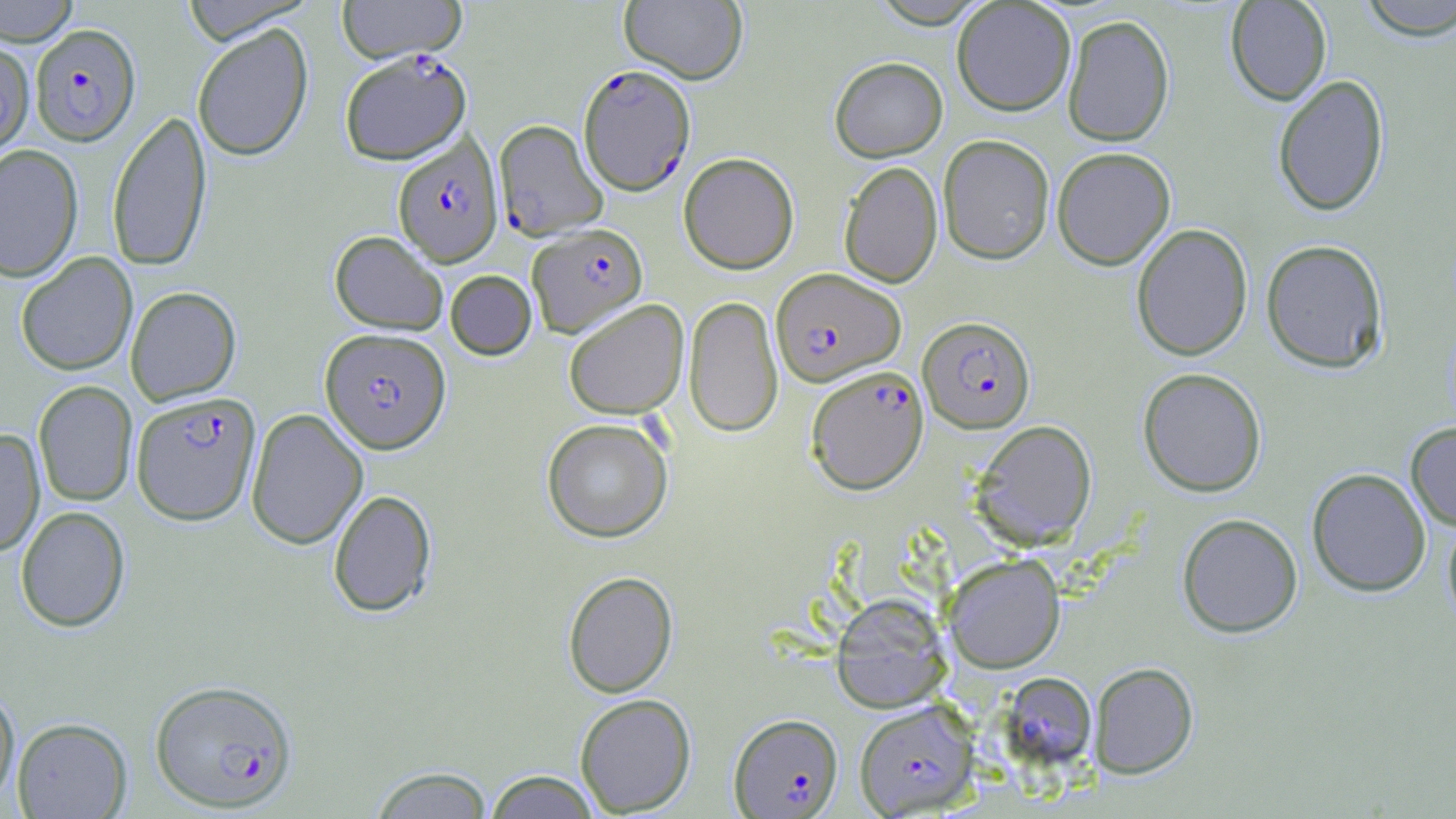

Approximate bounding boxes as named x1/y1/x2/y2 corners in pixels. Uninfected red blood cell locations: (x1=0, y1=0, x2=80, y2=45), (x1=336, y1=0, x2=466, y2=64), (x1=619, y1=0, x2=748, y2=84), (x1=869, y1=0, x2=992, y2=28), (x1=1225, y1=0, x2=1332, y2=105), (x1=1354, y1=0, x2=1456, y2=40), (x1=179, y1=1, x2=316, y2=45), (x1=952, y1=1, x2=1076, y2=116), (x1=1062, y1=14, x2=1175, y2=147), (x1=191, y1=24, x2=313, y2=161), (x1=0, y1=39, x2=35, y2=158), (x1=829, y1=56, x2=947, y2=162), (x1=1273, y1=74, x2=1389, y2=216), (x1=106, y1=109, x2=212, y2=272), (x1=938, y1=134, x2=1055, y2=264), (x1=0, y1=144, x2=83, y2=282), (x1=1052, y1=147, x2=1176, y2=270), (x1=678, y1=152, x2=799, y2=274), (x1=839, y1=161, x2=943, y2=288), (x1=1131, y1=223, x2=1253, y2=360), (x1=330, y1=231, x2=448, y2=335), (x1=1261, y1=239, x2=1388, y2=373), (x1=16, y1=252, x2=138, y2=376), (x1=445, y1=270, x2=537, y2=359), (x1=125, y1=286, x2=241, y2=405), (x1=683, y1=295, x2=783, y2=437), (x1=563, y1=299, x2=688, y2=419), (x1=1137, y1=367, x2=1266, y2=497), (x1=33, y1=380, x2=137, y2=506), (x1=246, y1=408, x2=368, y2=550), (x1=541, y1=418, x2=673, y2=542), (x1=970, y1=420, x2=1097, y2=550), (x1=1406, y1=422, x2=1456, y2=530), (x1=0, y1=428, x2=45, y2=556), (x1=1307, y1=468, x2=1431, y2=597), (x1=328, y1=489, x2=437, y2=617), (x1=15, y1=506, x2=130, y2=632), (x1=1177, y1=513, x2=1303, y2=638), (x1=1443, y1=514, x2=1456, y2=632), (x1=945, y1=553, x2=1065, y2=673), (x1=563, y1=570, x2=678, y2=698), (x1=831, y1=593, x2=951, y2=712), (x1=1089, y1=662, x2=1199, y2=778), (x1=998, y1=671, x2=1098, y2=772), (x1=0, y1=685, x2=19, y2=809), (x1=575, y1=694, x2=696, y2=816), (x1=12, y1=717, x2=132, y2=818), (x1=367, y1=765, x2=496, y2=818), (x1=482, y1=770, x2=603, y2=818). Plasmodium falciparum-infected red blood cell locations: (x1=29, y1=23, x2=141, y2=146), (x1=339, y1=49, x2=473, y2=165), (x1=578, y1=64, x2=695, y2=196), (x1=494, y1=119, x2=607, y2=240), (x1=393, y1=135, x2=502, y2=267), (x1=528, y1=222, x2=648, y2=338), (x1=771, y1=268, x2=906, y2=386), (x1=919, y1=316, x2=1036, y2=433), (x1=321, y1=328, x2=451, y2=453), (x1=807, y1=365, x2=928, y2=495), (x1=131, y1=391, x2=261, y2=526), (x1=150, y1=678, x2=298, y2=812), (x1=854, y1=699, x2=979, y2=816), (x1=728, y1=713, x2=843, y2=817). Slide-level diagnosis: Plasmodium falciparum. Image is 1456×819 pixels. Thin blood film. Light microscopy. 1000x magnification. May-Grünwald-Giemsa stain. Single field of view.